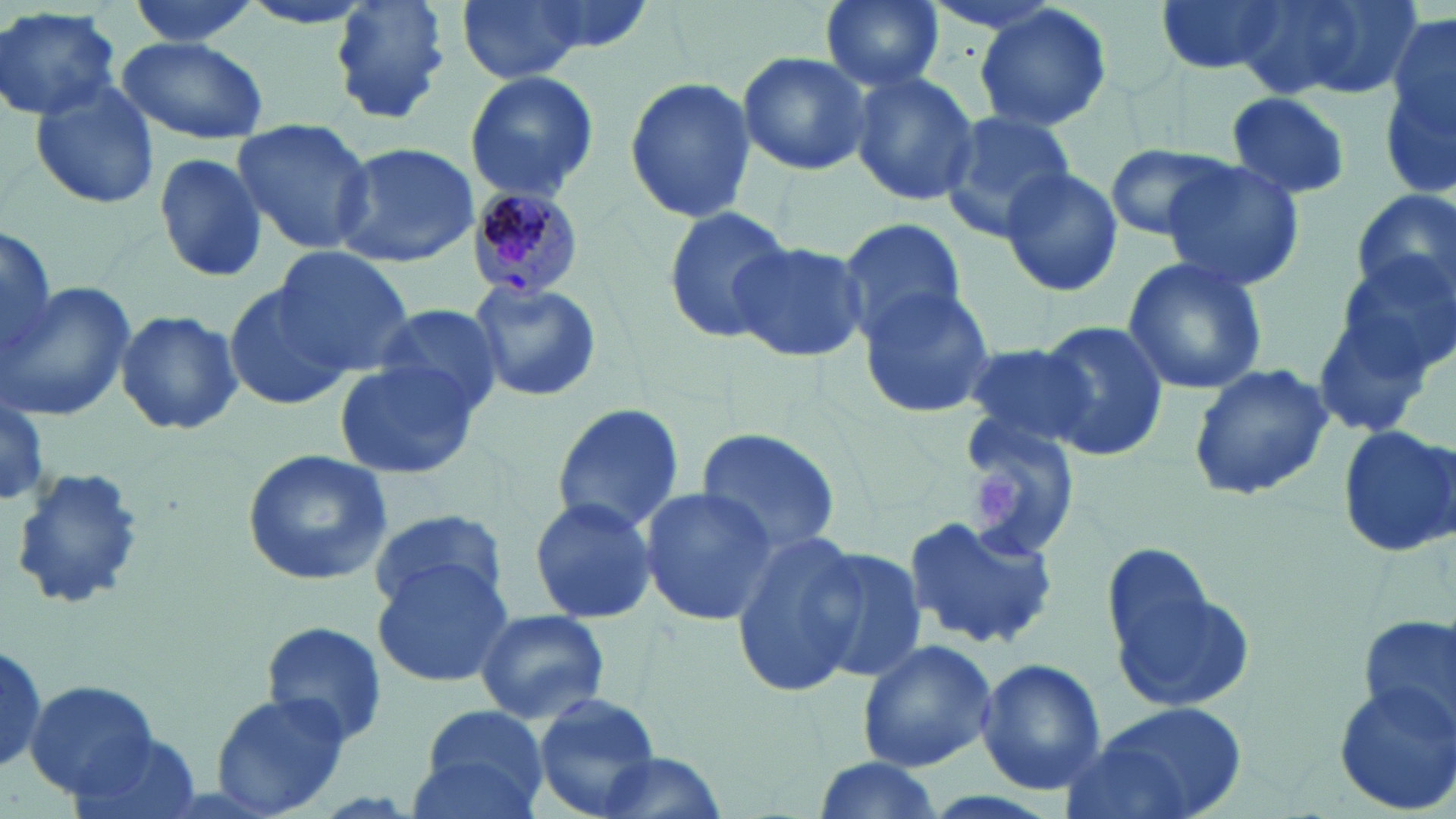
slide-level diagnosis = Plasmodium malariae
modality = light microscopy
preparation = thin blood smear
magnification = 1000x
platelet locations = approximate bounding boxes as (x1,y1)-(x2,y2) corner pairs in pixels: (970,467)-(1025,531)
field of view = single
uninfected red blood cell locations = approximate bounding boxes as (x1,y1)-(x2,y2) corner pairs in pixels: (123,0)-(265,49), (235,0)-(382,31), (331,0)-(451,120), (455,0)-(592,84), (819,0)-(945,92), (1153,0)-(1283,74), (1231,0)-(1418,103), (972,3)-(1114,134), (0,6)-(121,122), (1384,6)-(1456,198), (117,35)-(269,144), (737,52)-(872,177), (464,69)-(600,203), (849,71)-(979,207), (622,76)-(756,226), (28,78)-(159,209), (1224,91)-(1353,201), (942,109)-(1075,239), (229,119)-(377,253), (331,141)-(482,268), (1105,143)-(1235,242), (150,152)-(267,285), (1157,156)-(1306,292), (999,164)-(1123,298), (1351,188)-(1456,309), (660,206)-(795,341), (836,214)-(969,343), (1,224)-(57,368), (727,238)-(866,362), (271,247)-(413,370), (1330,253)-(1456,381), (1122,254)-(1270,397), (467,280)-(601,402), (0,281)-(135,422), (225,281)-(351,411), (857,282)-(996,419), (1308,284)-(1446,443), (374,301)-(505,418), (113,310)-(242,437), (1037,319)-(1170,463), (959,339)-(1097,453), (332,359)-(481,480), (1187,363)-(1334,505), (0,402)-(49,504), (550,402)-(684,536), (958,414)-(1083,558), (1337,423)-(1456,557), (694,427)-(844,558), (242,449)-(392,585), (8,466)-(150,613), (638,485)-(777,625), (526,494)-(658,626), (368,509)-(508,614), (904,512)-(1060,651), (728,534)-(870,693), (803,546)-(929,685), (372,556)-(516,686), (1108,568)-(1256,718), (472,607)-(610,723), (1356,615)-(1455,741), (259,620)-(391,748), (857,638)-(997,771), (0,641)-(48,776), (976,657)-(1107,797), (26,679)-(162,801), (1330,679)-(1456,814), (210,693)-(352,816), (534,694)-(663,817), (1067,703)-(1251,819), (412,705)-(549,817), (66,731)-(206,819), (593,752)-(727,819), (808,756)-(946,819)
white blood cell locations = approximate bounding boxes as (x1,y1)-(x2,y2) corner pairs in pixels: (11,466)-(151,618)
image size = 1456×819 pixels
Plasmodium malariae-infected red blood cell locations = approximate bounding boxes as (x1,y1)-(x2,y2) corner pairs in pixels: (464,185)-(586,297)
stain = May-Grünwald-Giemsa